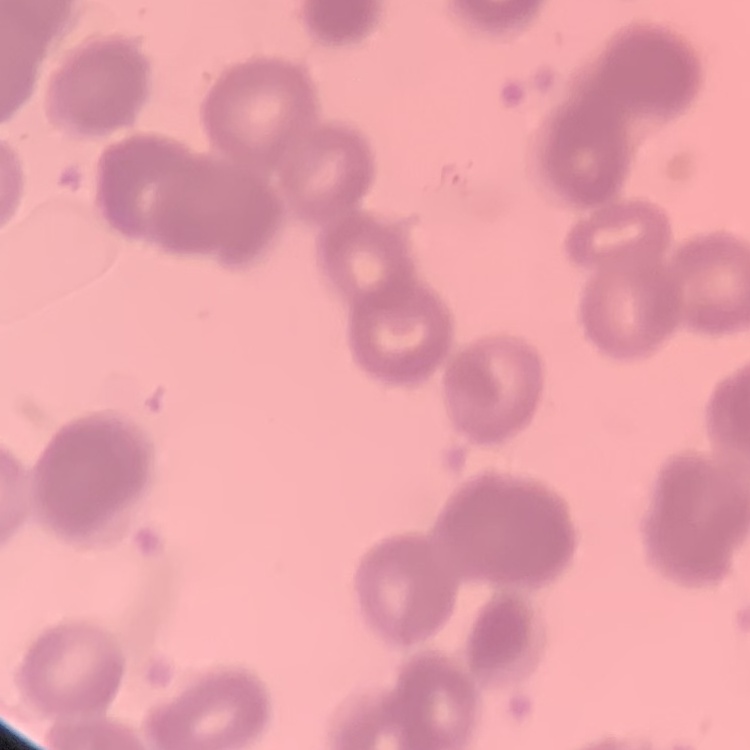 The red blood cells exhibit rouleaux formation. Stained with either Field's or Giemsa. Thin peripheral smear. One tile cut from a larger photomicrograph.